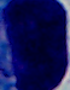 Captured at 1000x magnification. Micrograph. A white blood cell is seen.